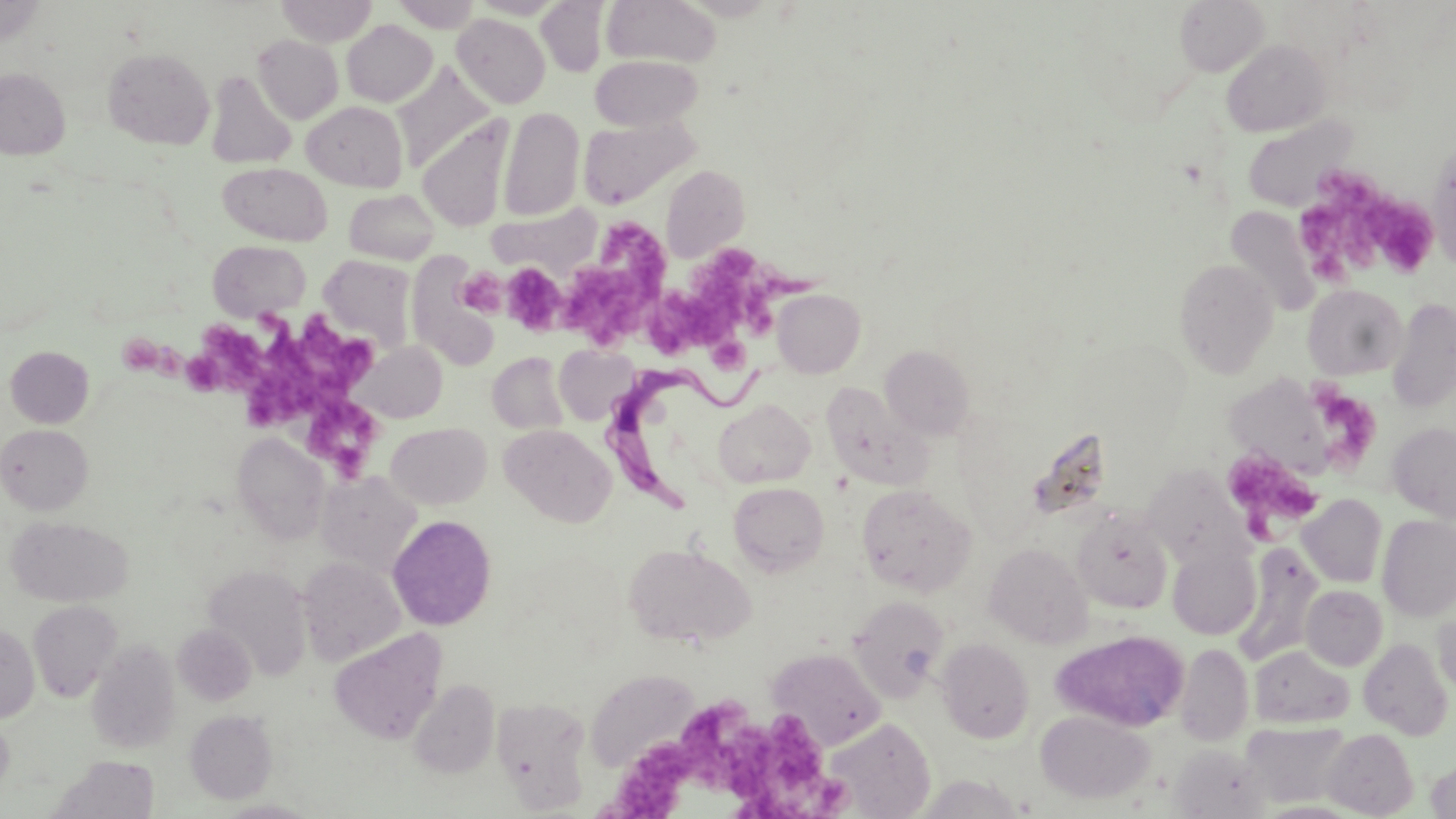
slide-level diagnosis = Trypanosoma brucei
stain = May-Grünwald-Giemsa
Trypanosoma brucei locations = approximate bounding boxes as [x1, y1, x2, y2] in pixels: [602, 366, 782, 514]
field of view = single
modality = optical microscopy
preparation = thin blood film
image size = 1456×819 pixels
magnification = 1000x
platelet locations = approximate bounding boxes as [x1, y1, x2, y2] in pixels: [1241, 114, 1358, 211], [1298, 167, 1396, 286], [1370, 199, 1438, 277], [599, 216, 674, 290], [692, 250, 811, 332], [502, 262, 566, 334], [567, 266, 649, 341], [457, 267, 509, 316], [643, 287, 736, 356], [202, 316, 354, 434], [706, 336, 748, 375], [119, 340, 161, 375], [166, 348, 222, 392], [1317, 377, 1380, 474], [306, 401, 379, 482], [1228, 450, 1317, 545], [674, 695, 757, 792], [727, 715, 851, 819], [597, 741, 698, 819]
uninfected red blood cell locations = approximate bounding boxes as [x1, y1, x2, y2] in pixels: [276, 0, 377, 46], [390, 0, 483, 31], [601, 0, 722, 67], [1174, 0, 1269, 76], [537, 1, 608, 76], [0, 3, 44, 46], [452, 13, 550, 108], [342, 20, 438, 106], [253, 34, 344, 124], [1221, 39, 1330, 137], [102, 47, 215, 149], [590, 55, 703, 131], [393, 63, 495, 169], [0, 67, 70, 159], [205, 71, 297, 169], [302, 101, 408, 191], [498, 108, 584, 221], [578, 115, 699, 209], [417, 117, 513, 231], [1428, 143, 1456, 272], [218, 162, 332, 245], [660, 164, 750, 261], [344, 188, 440, 265], [487, 203, 602, 276], [1225, 206, 1320, 316], [208, 240, 311, 320], [319, 255, 417, 353], [407, 257, 501, 370], [1175, 258, 1279, 378], [1303, 284, 1407, 379], [772, 289, 866, 377], [1386, 298, 1456, 412], [353, 341, 447, 423], [554, 344, 637, 424], [880, 345, 976, 440], [5, 346, 94, 428], [487, 352, 568, 435], [1231, 373, 1331, 479], [821, 381, 928, 490], [712, 399, 815, 488], [386, 421, 491, 510], [1387, 422, 1456, 522], [1, 424, 93, 514], [500, 424, 617, 527], [232, 432, 330, 545], [1143, 466, 1248, 567], [316, 470, 422, 576], [728, 482, 829, 576], [856, 484, 976, 596], [1298, 494, 1387, 588], [1073, 510, 1172, 613], [1377, 514, 1456, 622], [387, 515, 497, 630], [6, 516, 133, 607], [985, 543, 1093, 647], [1236, 543, 1322, 662], [624, 544, 755, 647], [1167, 544, 1261, 640], [297, 556, 405, 666], [203, 563, 313, 679], [1301, 585, 1387, 670], [848, 596, 948, 701], [28, 600, 123, 702], [1432, 609, 1456, 700], [0, 624, 39, 723], [173, 624, 256, 705], [330, 628, 448, 744], [1050, 629, 1191, 731], [1359, 637, 1452, 740], [937, 638, 1034, 743], [87, 640, 181, 753], [1175, 643, 1253, 746], [1249, 646, 1354, 728], [767, 647, 886, 749], [586, 668, 699, 772], [409, 678, 499, 778], [491, 697, 592, 813], [185, 709, 278, 804], [1036, 709, 1155, 804], [0, 712, 13, 796], [822, 717, 935, 817], [1242, 721, 1353, 807], [1322, 729, 1418, 817], [1169, 744, 1272, 819], [47, 756, 160, 819], [1425, 758, 1456, 817]